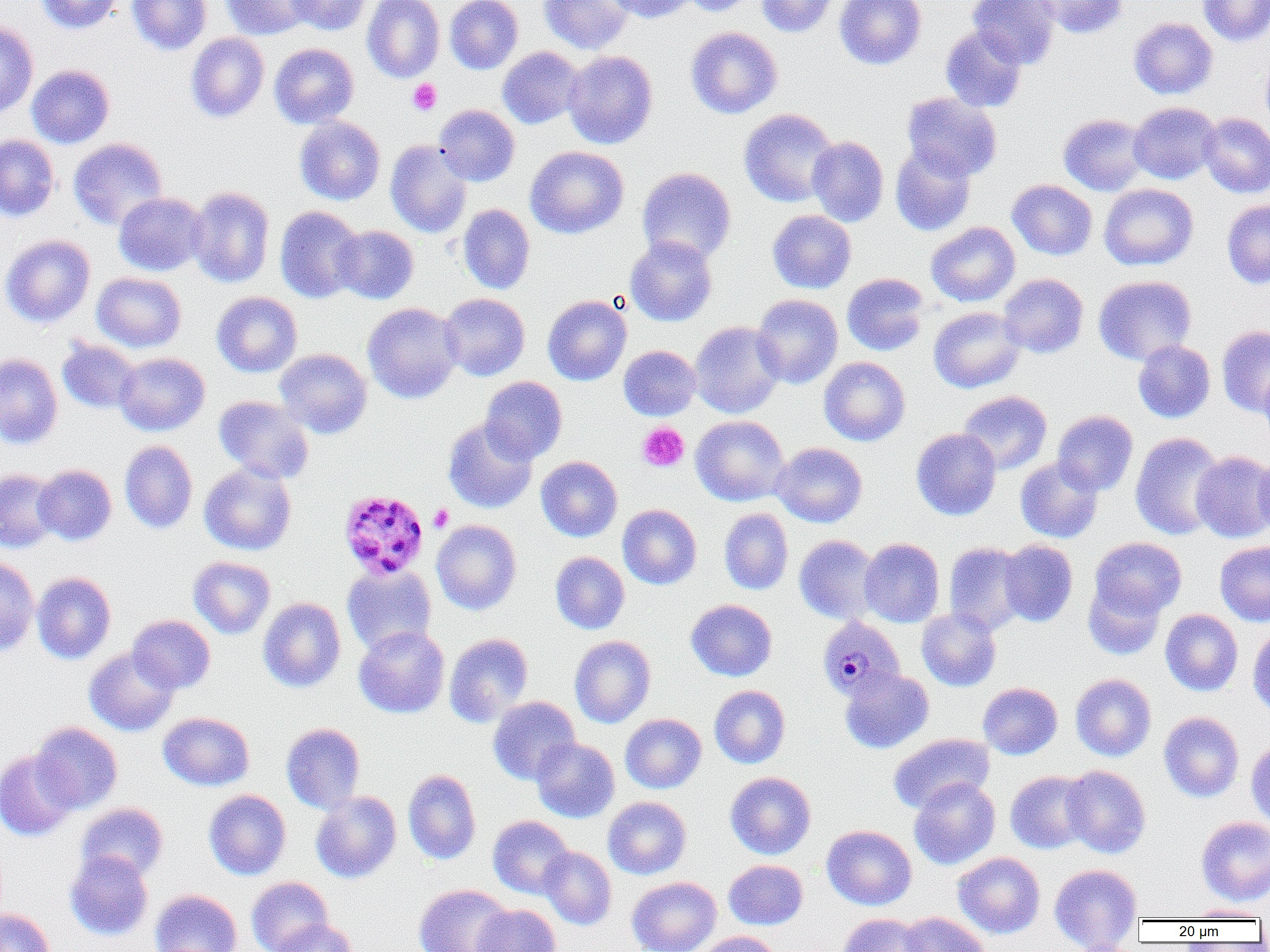
{
  "slide_level_diagnosis": "Plasmodium malariae",
  "preparation": "thin blood film",
  "plasmodium_malariae_infected_red_blood_cell_locations": "approximate bounding boxes as [x1, y1, x2, y2] in pixels: [338, 490, 429, 580], [817, 616, 905, 702]",
  "magnification": "1000x",
  "uninfected_red_blood_cell_locations": "approximate bounding boxes as [x1, y1, x2, y2] in pixels: [35, 0, 122, 34], [127, 0, 212, 55], [221, 0, 315, 40], [286, 0, 372, 35], [362, 0, 445, 83], [445, 0, 523, 74], [539, 0, 634, 54], [607, 0, 696, 23], [682, 0, 760, 16], [756, 0, 839, 37], [835, 0, 926, 69], [968, 0, 1061, 69], [1031, 0, 1128, 39], [1197, 0, 1270, 46], [1129, 17, 1218, 99], [0, 22, 38, 119], [940, 25, 1028, 113], [685, 26, 783, 119], [185, 33, 269, 123], [269, 43, 358, 128], [497, 47, 584, 129], [563, 50, 658, 149], [1261, 51, 1270, 134], [26, 64, 115, 148], [902, 92, 1002, 181], [1128, 102, 1222, 184], [433, 104, 520, 186], [739, 109, 838, 207], [1058, 113, 1150, 196], [1199, 113, 1270, 198], [294, 116, 385, 205], [0, 135, 59, 221], [807, 136, 889, 227], [68, 137, 168, 230], [385, 140, 472, 238], [890, 145, 976, 236], [526, 146, 629, 239], [637, 167, 736, 264], [1007, 179, 1097, 260], [1099, 183, 1199, 271], [188, 186, 275, 288], [113, 192, 208, 276], [1222, 200, 1270, 289], [457, 204, 535, 294], [274, 206, 365, 303], [767, 210, 856, 294], [926, 221, 1020, 306], [331, 225, 419, 304], [0, 234, 95, 328], [624, 235, 718, 326], [92, 272, 186, 352], [842, 273, 930, 356], [998, 273, 1088, 358], [1093, 275, 1197, 365], [212, 292, 302, 377], [439, 293, 530, 381], [752, 294, 843, 389], [543, 295, 631, 386], [362, 302, 463, 403], [928, 306, 1026, 393], [690, 321, 785, 418], [1217, 325, 1270, 416], [57, 338, 142, 413], [1133, 340, 1215, 423], [619, 345, 701, 420], [274, 348, 372, 438], [114, 352, 210, 436], [0, 353, 63, 449], [819, 357, 911, 446], [1259, 365, 1270, 451], [480, 377, 568, 463], [957, 390, 1052, 474], [214, 395, 315, 483], [1052, 410, 1138, 495], [691, 415, 789, 506], [442, 418, 538, 514], [911, 428, 1001, 520], [1130, 432, 1226, 539], [119, 440, 198, 533], [771, 442, 867, 527], [1191, 451, 1270, 542], [1254, 455, 1270, 538], [536, 456, 623, 542], [1015, 456, 1103, 543], [199, 463, 297, 555], [33, 464, 116, 546], [0, 469, 60, 553], [617, 504, 702, 590], [719, 508, 793, 594], [431, 519, 521, 615], [794, 535, 881, 624], [1090, 537, 1186, 619], [859, 538, 944, 627], [998, 540, 1078, 627], [1215, 541, 1270, 626], [944, 542, 1029, 635], [550, 551, 630, 634], [188, 556, 276, 638], [0, 557, 40, 656], [342, 565, 437, 655], [32, 572, 116, 664], [1083, 580, 1167, 660], [258, 597, 346, 692], [686, 599, 777, 681], [916, 608, 1002, 691], [1160, 609, 1243, 695], [128, 615, 215, 694], [353, 626, 450, 718], [1247, 626, 1270, 718], [444, 633, 534, 727], [569, 636, 656, 728], [84, 647, 179, 736], [840, 668, 934, 753], [1070, 673, 1156, 761], [978, 682, 1062, 759], [709, 685, 790, 768], [488, 696, 581, 785], [1159, 711, 1244, 802], [158, 712, 254, 791], [617, 713, 699, 880], [620, 714, 707, 793], [31, 722, 123, 814], [281, 723, 365, 814], [888, 732, 994, 814], [531, 737, 620, 822], [1246, 738, 1270, 827], [0, 750, 77, 841], [1061, 765, 1151, 859], [402, 769, 481, 865], [1005, 770, 1093, 854], [725, 771, 816, 859], [909, 777, 1000, 869], [203, 789, 291, 880], [311, 791, 401, 883], [603, 796, 691, 879], [76, 802, 168, 882], [488, 815, 573, 898], [1196, 816, 1270, 906], [821, 825, 916, 910], [538, 846, 617, 930], [65, 850, 153, 941], [953, 852, 1045, 938], [723, 859, 808, 930], [1049, 864, 1142, 949], [246, 876, 333, 952], [627, 876, 721, 952], [414, 884, 514, 952], [149, 888, 242, 952], [471, 903, 561, 952], [1184, 904, 1269, 920], [0, 907, 55, 952], [899, 911, 992, 952], [837, 913, 928, 952], [271, 919, 356, 952], [691, 931, 780, 952]",
  "field_of_view": "single",
  "image_size": "1270×952 pixels",
  "platelet_locations": "approximate bounding boxes as [x1, y1, x2, y2] in pixels: [407, 79, 441, 116], [637, 423, 689, 472], [428, 504, 453, 532]",
  "modality": "light microscopy"
}